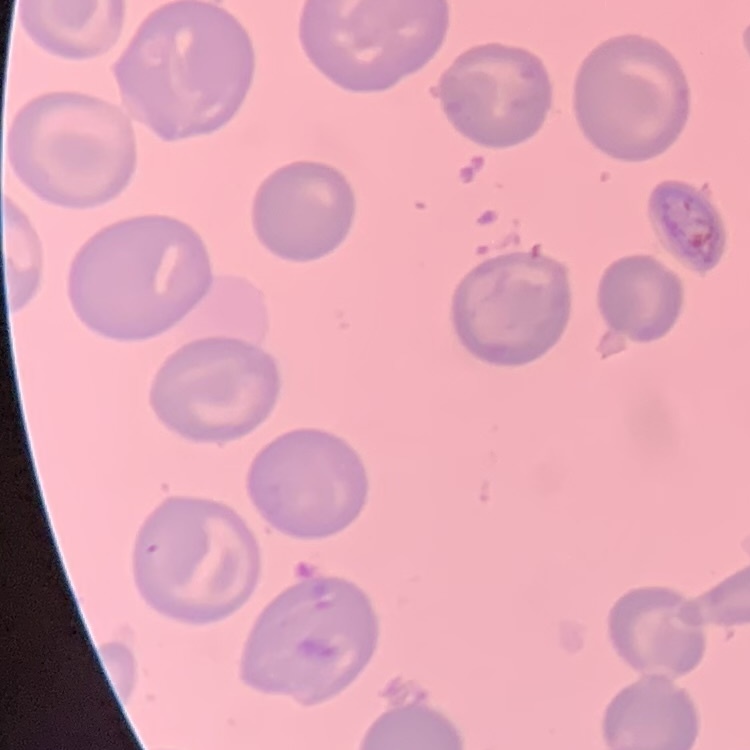
The erythrocytes show no rouleaux formation. One tile cut from a larger photomicrograph. Thin blood film. Stained with either Field's or Giemsa.